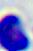
modality = micrograph
identification = leukocyte
magnification = 400x